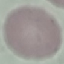

Summary:
  - Result: no malaria parasites seen
  - Stain: Giemsa
  - Preparation: thin smear
  - Capture: smartphone through the microscope eyepiece
  - Image type: automatically extracted cell patch, resized to 64 × 64 pixels